Draw a bounding box around every leukocyte (white blood cell).
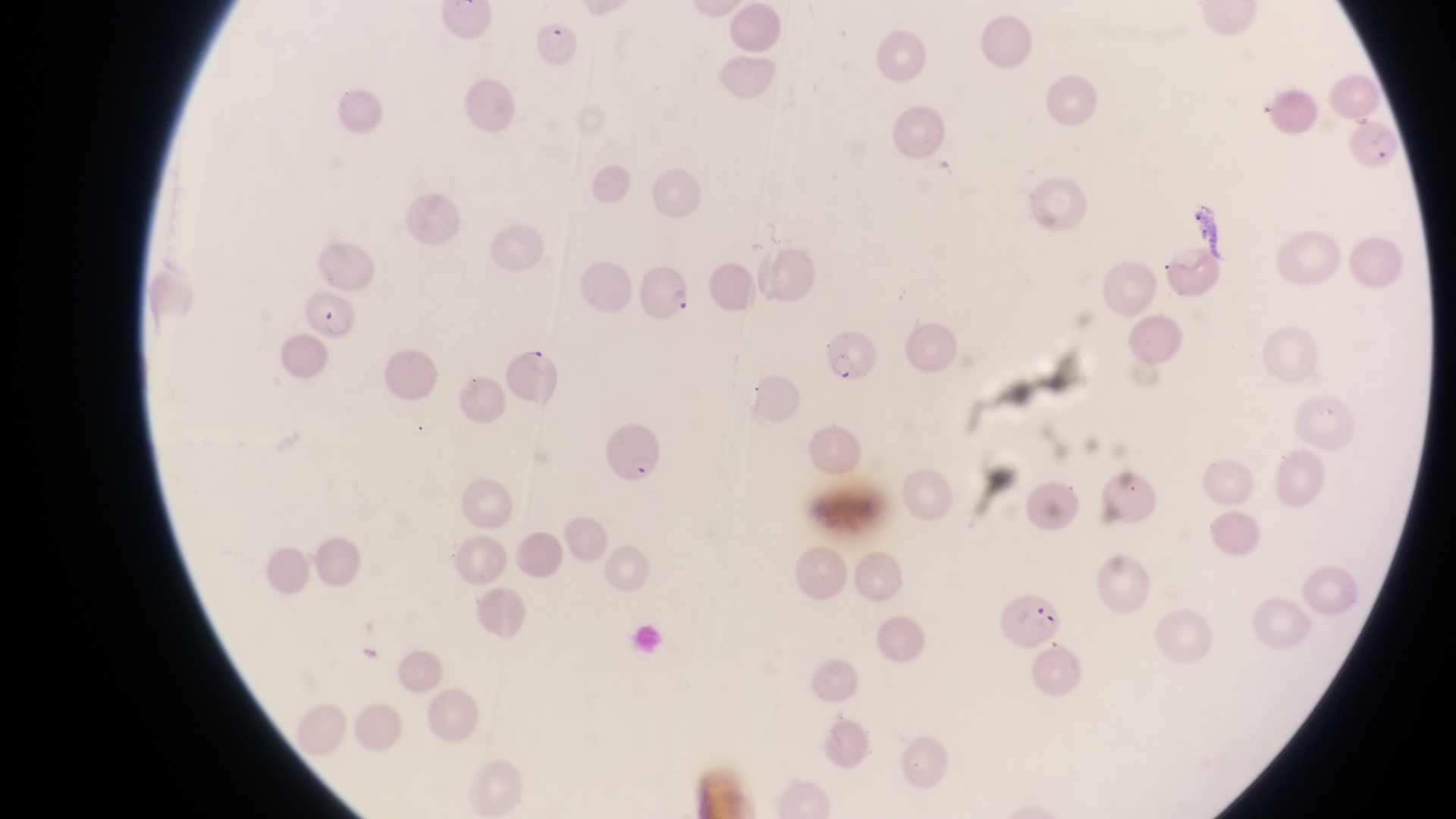

No leukocytes observed.

Approximate bounding boxes as (left, top, right, bottom) in pixels.
Summary:
  - Parasitised red blood cell locations: (532, 22, 581, 71), (639, 265, 694, 326), (306, 288, 362, 344), (827, 327, 880, 385), (507, 346, 566, 409), (598, 423, 664, 486), (1004, 591, 1064, 652)
  - Field of view: single
  - Image size: 1456×819 pixels
  - Magnification: 1000x
  - Country: Uganda
  - Preparation: thin blood film
  - Capture: smartphone photograph through the eyepiece of an Olympus CX-23 microscope